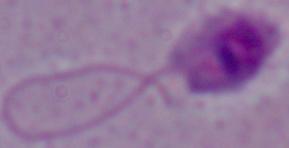
Summary:
  - Modality: micrograph
  - Magnification: 1000x
  - Identification: Leishmania